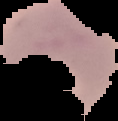
Malaria status: parasitized. Segmented cell region on a black background. Image is 118×121 pixels. From a thin blood smear.